Give the position of every Plasmodium parasite.
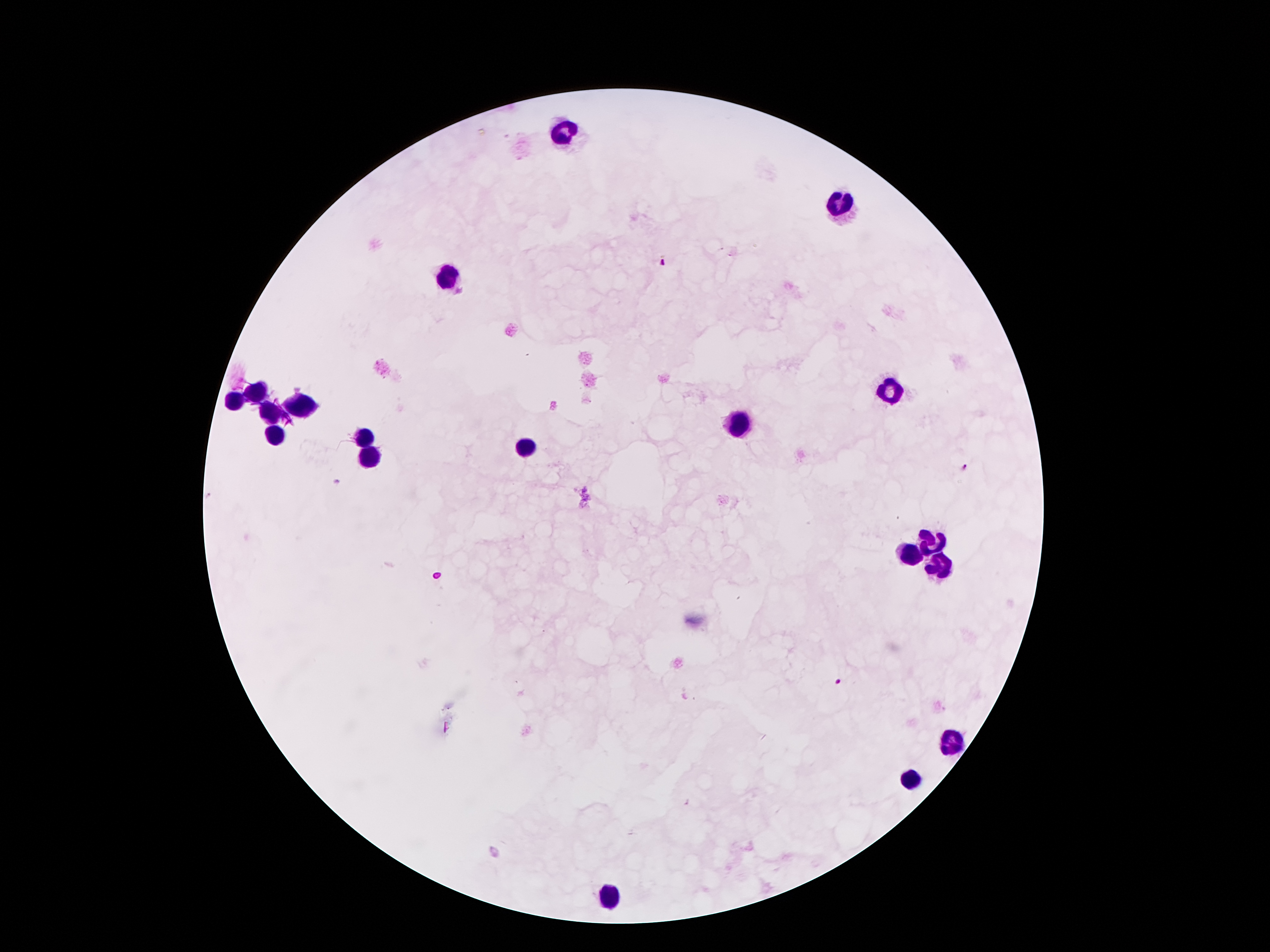
Approximate centers as {x, y} in pixels.
Plasmodium parasites: {661, 263}, {964, 468}, {840, 681}.

leukocyte locations = {563, 129}, {838, 209}, {447, 278}, {256, 389}, {889, 391}, {231, 404}, {296, 408}, {269, 419}, {735, 427}, {273, 435}, {366, 437}, {523, 448}, {368, 456}, {933, 545}, {912, 553}, {939, 563}, {952, 744}, {910, 780}, {611, 897}
magnification = 100x
capture = smartphone camera through the microscope eyepiece
stain = Giemsa
image size = 1270×952 pixels
field of view = one from this slide
patient malaria status = positive for Plasmodium falciparum
preparation = thick peripheral-blood smear